Point out every Plasmodium parasite and every leukocyte.
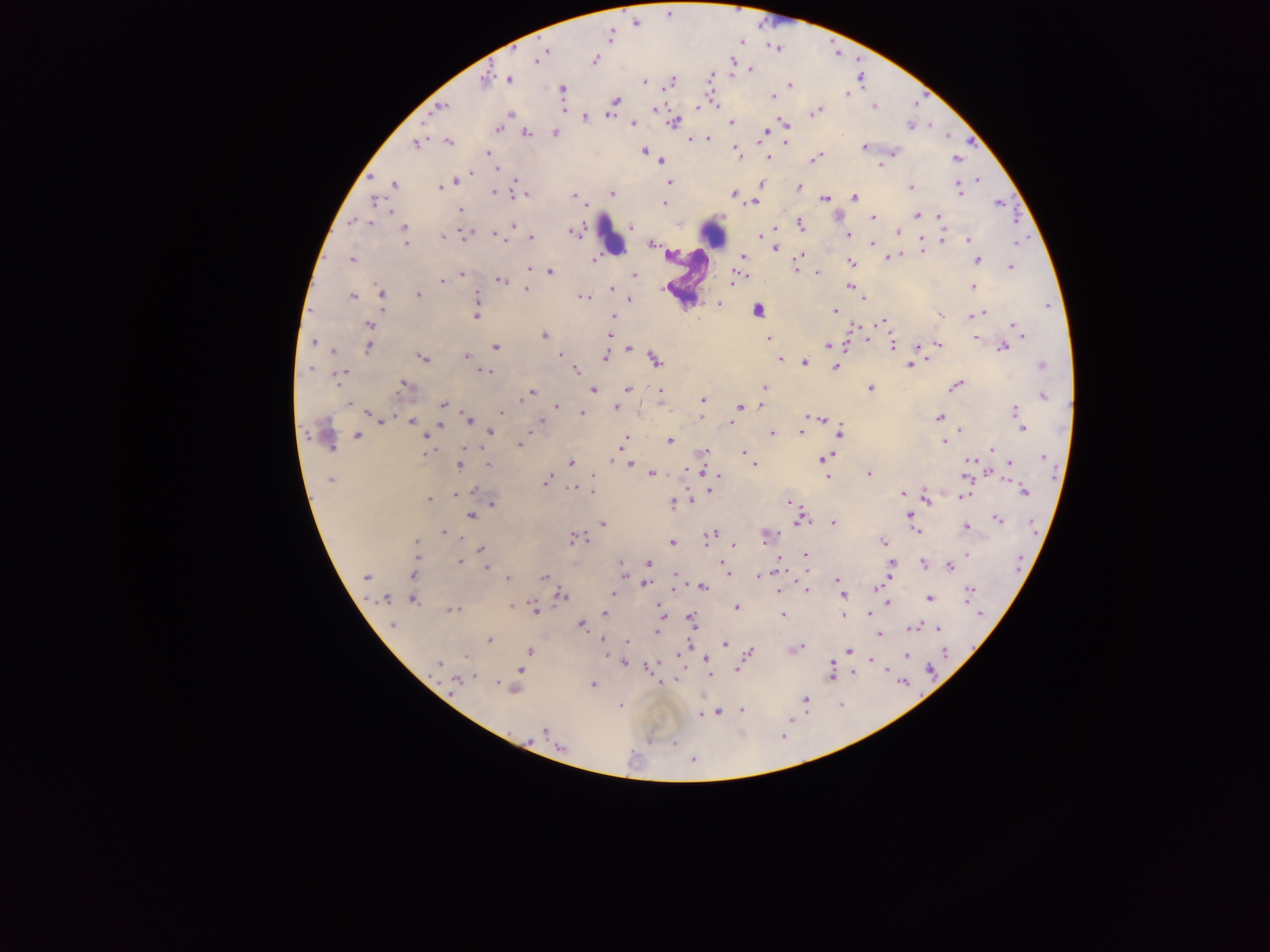

Approximate centers as x y in pixels.
Plasmodium parasites: 609 36; 544 52; 539 57; 595 60; 751 69; 710 78; 510 79; 484 80; 644 81; 671 81; 790 84; 562 89; 848 93; 773 96; 616 101; 443 106; 874 107; 697 108; 655 109; 818 111; 509 114; 609 114; 585 117; 674 122; 785 123; 633 124; 732 124; 910 126; 498 128; 764 131; 527 133; 554 133; 708 139; 691 140; 785 142; 449 143; 416 144; 864 147; 644 151; 737 151; 486 152; 894 152; 767 158; 815 159; 956 159; 663 161; 880 164; 497 168; 472 173; 978 180; 516 181; 456 182; 669 182; 394 184; 761 184; 799 187; 440 188; 910 188; 959 189; 495 193; 612 193; 734 194; 525 195; 573 196; 854 198; 825 199; 375 200; 665 203; 753 203; 998 203; 460 210; 391 211; 917 215; 938 217; 873 218; 355 221; 369 223; 801 224; 512 226; 632 226; 900 228; 404 229; 898 231; 573 232; 848 234; 761 235; 466 236; 498 237; 442 238; 531 239; 942 240; 969 240; 405 242; 871 243; 1015 244; 651 245; 776 248; 923 250; 800 256; 742 257; 890 257; 351 259; 594 259; 977 261; 850 262; 797 265; 1011 267; 529 268; 797 271; 551 272; 817 273; 462 275; 741 275; 633 276; 734 279; 441 281; 501 282; 849 286; 973 286; 527 289; 612 289; 382 294; 419 295; 352 296; 477 296; 585 299; 630 299; 863 299; 718 304; 835 311; 982 313; 940 315; 973 315; 476 316; 614 316; 883 321; 369 325; 1016 328; 610 333; 544 335; 976 338; 768 339; 314 342; 938 344; 829 345; 892 345; 919 346; 369 347; 496 347; 1004 347; 629 349; 333 351; 559 354; 605 356; 466 357; 423 358; 656 359; 780 359; 804 363; 909 365; 1042 366; 835 367; 311 369; 575 371; 484 372; 340 374; 404 384; 956 385; 764 388; 871 388; 627 389; 594 390; 660 391; 531 392; 1044 396; 527 397; 703 399; 520 401; 349 403; 443 404; 760 405; 556 407; 740 407; 615 408; 1016 410; 501 413; 370 414; 581 414; 939 417; 818 418; 1019 419; 382 420; 468 420; 411 421; 541 421; 733 423; 1022 428; 961 430; 491 432; 840 432; 801 433; 773 434; 357 435; 425 438; 624 440; 670 442; 944 442; 519 445; 428 450; 992 450; 704 452; 744 453; 748 455; 1043 457; 824 459; 612 460; 571 463; 970 463; 630 464; 1010 464; 489 465; 753 465; 459 466; 634 466; 700 469; 652 474; 593 475; 869 475; 717 476; 828 477; 331 480; 545 481; 573 489; 1023 490; 471 491; 591 492; 456 493; 902 493; 965 495; 926 496; 429 499; 673 502; 790 502; 493 504; 471 516; 909 516; 998 519; 800 521; 603 524; 833 524; 914 526; 966 527; 916 531; 444 532; 712 533; 766 537; 574 538; 416 541; 672 542; 883 542; 733 545; 481 549; 806 555; 460 561; 621 563; 649 563; 923 563; 891 566; 950 566; 487 568; 726 568; 622 573; 412 574; 759 576; 544 577; 366 578; 508 578; 837 581; 646 584; 703 587; 879 587; 807 590; 779 592; 969 592; 612 594; 561 595; 843 595; 929 598; 385 599; 413 601; 888 603; 512 607; 738 607; 534 609; 454 610; 660 611; 605 613; 870 613; 783 615; 843 616; 692 619; 393 624; 581 624; 913 627; 938 628; 656 632; 879 634; 489 640; 602 641; 626 642; 724 643; 688 646; 796 650; 529 651; 848 651; 606 652; 749 652; 906 655; 466 657; 706 660; 872 661; 438 663; 623 663; 648 668; 738 669; 521 670; 831 672; 855 673; 709 674; 473 677; 456 682; 498 684; 594 684; 513 690; 805 699; 620 706; 742 710; 718 713; 700 715; 544 732; 674 743; 562 748; 694 761.
Leukocytes: 713 233; 612 236; 760 310.

Mobile-phone photograph taken through the microscope. Collected in Ghana. Thick blood smear. Single field of view. Image is 1270×952 pixels.